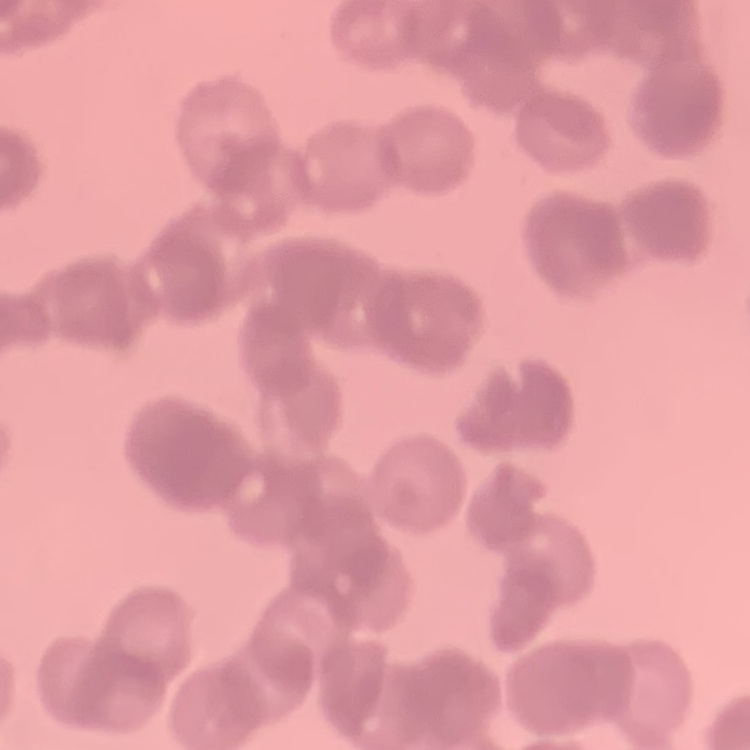

Summary:
  - Erythrocyte morphology: rouleaux formation
  - Image type: one tile cut from a larger photomicrograph
  - Preparation: thin blood film
  - Stain: Field's or Giemsa